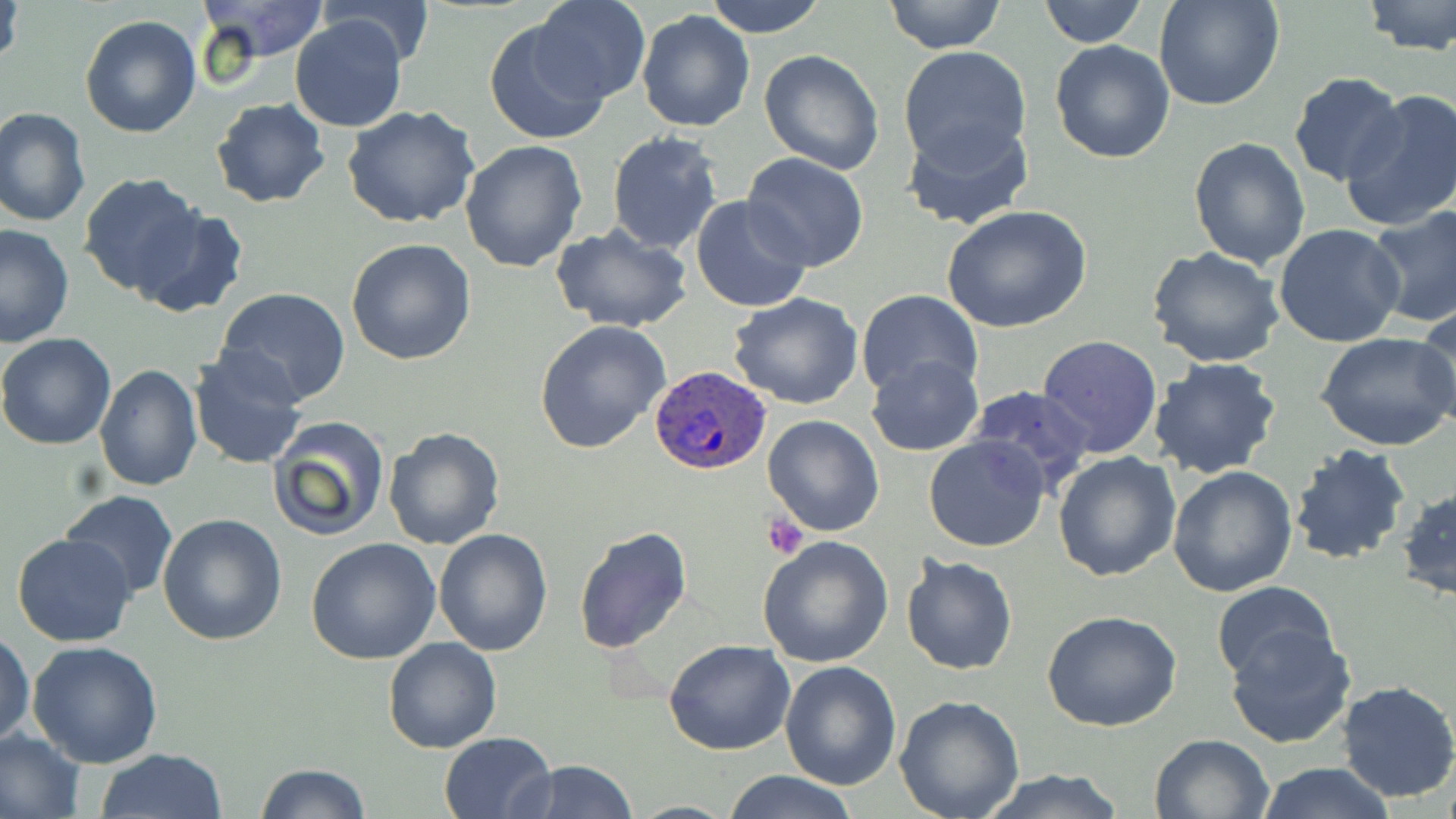
slide-level diagnosis = Plasmodium ovale
field of view = one of a larger specimen
preparation = thin blood film
Plasmodium ovale-infected red blood cell locations = approximate bounding boxes as [x1, y1, x2, y2] in pixels: [648, 364, 772, 476]
uninfected red blood cell locations = approximate bounding boxes as [x1, y1, x2, y2] in pixels: [1, 0, 25, 74], [198, 0, 331, 64], [528, 0, 651, 105], [704, 0, 829, 38], [883, 0, 1006, 53], [1039, 0, 1145, 47], [1154, 0, 1286, 111], [1361, 0, 1456, 56], [321, 1, 434, 66], [637, 9, 754, 132], [79, 14, 202, 138], [290, 14, 410, 133], [485, 16, 612, 145], [1049, 39, 1176, 164], [898, 46, 1034, 170], [760, 48, 887, 175], [1287, 73, 1407, 189], [1340, 89, 1456, 232], [209, 98, 330, 207], [341, 104, 480, 230], [0, 107, 91, 228], [901, 115, 1034, 232], [606, 129, 726, 256], [1190, 137, 1310, 268], [460, 139, 588, 272], [740, 153, 869, 273], [78, 173, 206, 298], [692, 195, 812, 313], [941, 204, 1094, 335], [1368, 205, 1456, 331], [130, 208, 248, 319], [0, 223, 74, 348], [549, 223, 694, 333], [1273, 224, 1406, 349], [345, 239, 477, 365], [1145, 245, 1286, 367], [214, 285, 351, 404], [856, 289, 982, 403], [728, 293, 864, 410], [1413, 304, 1456, 433], [535, 320, 670, 453], [1315, 331, 1456, 451], [0, 332, 117, 451], [1038, 335, 1163, 459], [187, 345, 309, 471], [866, 354, 983, 456], [1148, 357, 1282, 479], [93, 363, 203, 491], [966, 385, 1095, 494], [763, 414, 886, 537], [267, 415, 391, 542], [383, 426, 505, 550], [922, 436, 1051, 553], [1287, 444, 1412, 566], [1052, 450, 1182, 582], [1166, 465, 1298, 597], [1398, 484, 1456, 604], [59, 490, 179, 600], [158, 513, 289, 646], [573, 527, 693, 654], [433, 528, 553, 656], [11, 533, 137, 647], [756, 534, 896, 668], [305, 538, 441, 666], [899, 554, 1018, 676], [1210, 581, 1340, 688], [1042, 610, 1183, 731], [1226, 624, 1357, 749], [0, 631, 35, 749], [382, 637, 503, 753], [663, 639, 795, 755], [27, 641, 163, 769], [780, 660, 903, 790], [1336, 680, 1456, 803], [894, 695, 1025, 818], [0, 727, 86, 819], [438, 731, 556, 817], [1149, 733, 1276, 819], [95, 748, 227, 819], [519, 759, 638, 819], [1254, 762, 1397, 819], [253, 763, 369, 819], [973, 769, 1130, 819], [720, 771, 859, 819]
stain = May-Grünwald-Giemsa
magnification = 1000x
image size = 1456×819 pixels
platelet locations = approximate bounding boxes as [x1, y1, x2, y2] in pixels: [765, 513, 809, 560]
modality = light microscopy